Report the malaria status of this cell.
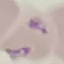

It is parasitized.

{
  "image_type": "automatically extracted cell patch, resized to 64 × 64 pixels",
  "capture": "smartphone camera at the microscope eyepiece",
  "preparation": "thin blood smear",
  "stain": "Giemsa"
}